Assess this cell for malaria.
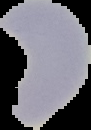

It is uninfected.

preparation = thin blood film
image size = 91×130 pixels
image type = segmented cell region on a black background